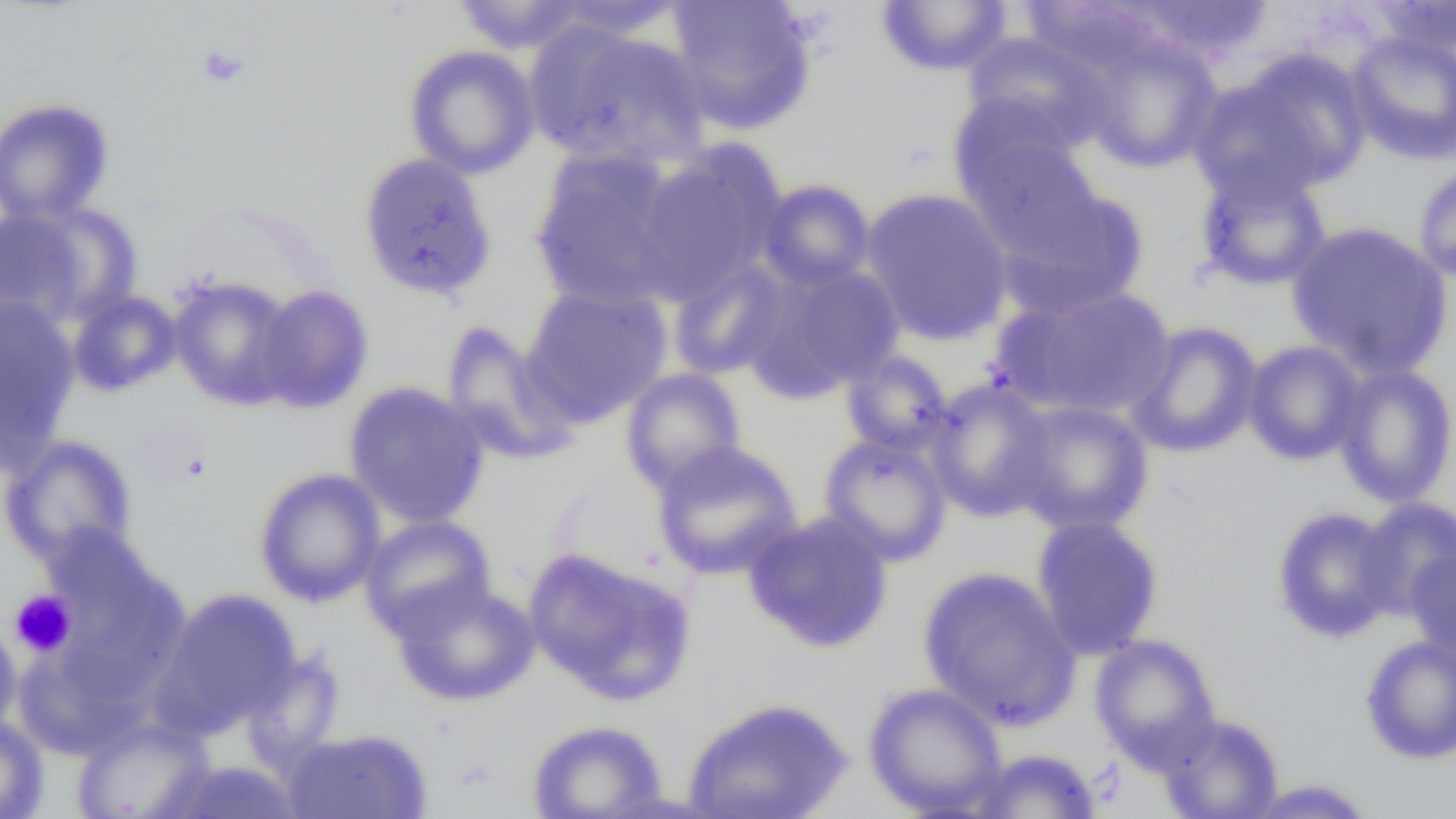
slide_level_diagnosis: negative for blood parasites
platelet_locations: 'approximate bounding boxes as (x1,y1)-(x2,y2) corner pairs in pixels: (197,44)-(248,88), (10,590)-(76,657)'
modality: light microscopy
preparation: thin blood smear
uninfected_red_blood_cell_locations: 'approximate bounding boxes as (x1,y1)-(x2,y2) corner pairs in pixels: (450,0)-(589,54), (666,0)-(817,134), (1120,0)-(1276,63), (1362,0)-(1456,57), (540,1)-(693,40), (875,1)-(1013,76), (530,26)-(712,171), (961,31)-(1113,153), (1346,31)-(1456,165), (1076,33)-(1224,174), (403,45)-(540,179), (1226,49)-(1374,194), (1187,75)-(1329,206), (950,92)-(1082,200), (0,98)-(114,225), (962,132)-(1105,259), (633,145)-(785,301), (529,151)-(688,311), (358,153)-(497,299), (1414,163)-(1456,284), (1194,165)-(1332,292), (756,179)-(876,290), (999,185)-(1150,317), (860,188)-(1013,345), (13,201)-(142,323), (1286,221)-(1453,379), (667,258)-(792,381), (747,262)-(906,399), (169,276)-(299,410), (520,283)-(673,424), (254,284)-(374,413), (992,284)-(1177,422), (68,291)-(182,397), (0,296)-(80,466), (440,321)-(580,465), (1125,321)-(1264,459), (1242,340)-(1366,466), (840,350)-(955,457), (1332,364)-(1456,508), (620,368)-(746,494), (924,378)-(1056,522), (343,381)-(489,528), (1009,400)-(1154,535), (818,433)-(953,566), (0,434)-(138,568), (651,440)-(802,581), (253,467)-(387,607), (1353,497)-(1456,622), (1271,506)-(1401,644), (743,510)-(894,652), (360,515)-(496,638), (1030,515)-(1164,660), (36,523)-(174,646), (1404,547)-(1456,663), (523,548)-(696,705), (46,560)-(193,707), (918,566)-(1081,730), (390,580)-(539,707), (154,589)-(301,735), (0,618)-(23,736), (1089,633)-(1222,772), (1360,634)-(1456,764), (12,643)-(148,761), (241,650)-(345,774), (863,682)-(1007,816), (682,696)-(853,819), (1157,712)-(1285,819), (0,715)-(48,819), (71,718)-(213,819), (527,719)-(668,819), (284,728)-(431,819), (967,748)-(1102,819), (163,760)-(304,819), (1241,779)-(1379,818)'
field_of_view: single
image_size: 1456×819 pixels
magnification: 1000x